Locate every Plasmodium falciparum-infected red blood cell.
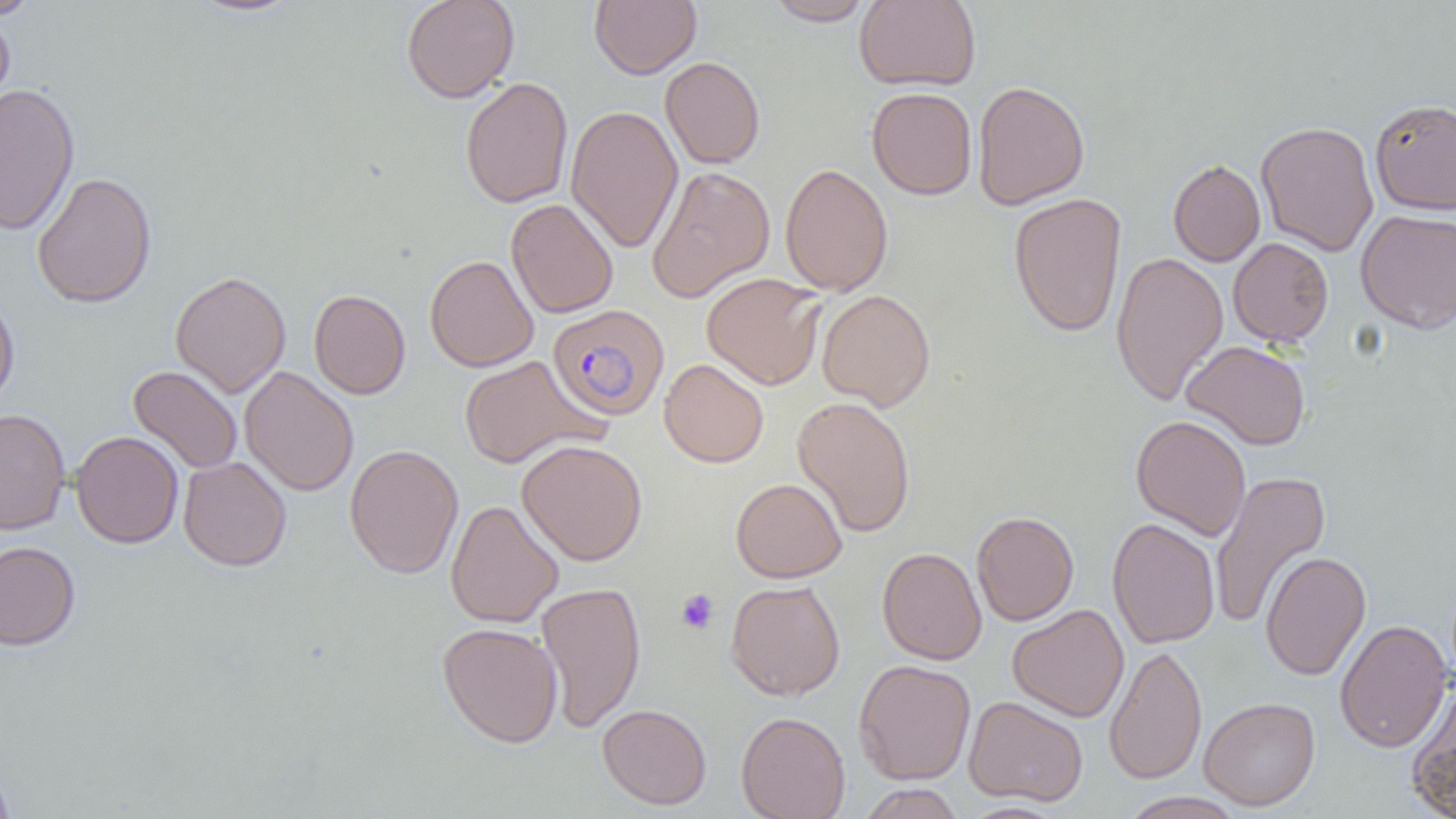

Approximate bounding boxes as [x1, y1, x2, y2] in pixels.
Plasmodium falciparum-infected red blood cells: [547, 304, 669, 422].

slide_level_diagnosis: Plasmodium falciparum
image_size: 1456×819 pixels
magnification: 1000x
uninfected_red_blood_cell_locations: 'approximate bounding boxes as [x1, y1, x2, y2] in pixels: [1, 0, 42, 20], [186, 0, 304, 17], [401, 0, 520, 103], [589, 0, 701, 79], [762, 0, 875, 26], [854, 0, 981, 91], [0, 9, 16, 114], [660, 56, 765, 169], [460, 77, 573, 209], [972, 81, 1090, 210], [0, 83, 80, 236], [866, 87, 977, 200], [1369, 99, 1456, 215], [566, 104, 683, 254], [1255, 120, 1379, 257], [1168, 159, 1265, 267], [780, 163, 893, 296], [646, 164, 775, 302], [32, 171, 157, 309], [1008, 192, 1127, 338], [506, 198, 618, 319], [1355, 209, 1456, 335], [1228, 237, 1334, 346], [1111, 251, 1228, 407], [424, 254, 539, 372], [170, 271, 291, 398], [701, 272, 826, 391], [309, 289, 411, 399], [817, 289, 936, 411], [0, 291, 20, 408], [1181, 340, 1310, 450], [459, 355, 603, 469], [658, 358, 769, 468], [127, 365, 243, 475], [239, 366, 359, 497], [791, 396, 916, 538], [0, 408, 70, 535], [1131, 415, 1251, 541], [70, 430, 183, 549], [516, 439, 648, 566], [72, 444, 291, 556], [344, 444, 464, 579], [178, 456, 292, 571], [1210, 470, 1330, 630], [731, 478, 847, 583], [445, 499, 563, 629], [971, 510, 1079, 626], [1107, 518, 1220, 649], [0, 541, 80, 651], [877, 547, 987, 665], [1260, 550, 1371, 681], [725, 579, 845, 701], [535, 581, 647, 733], [1007, 604, 1129, 722], [1334, 619, 1453, 752], [437, 622, 563, 747], [1104, 644, 1207, 785], [853, 659, 975, 785], [1405, 684, 1456, 818], [963, 695, 1088, 806], [1199, 696, 1320, 811], [597, 704, 712, 810], [736, 711, 850, 819], [0, 762, 16, 819], [856, 784, 965, 819], [1118, 791, 1247, 819], [956, 801, 1069, 819]'
platelet_locations: 'approximate bounding boxes as [x1, y1, x2, y2] in pixels: [676, 588, 719, 634]'
field_of_view: one of a larger specimen
modality: optical microscopy
preparation: thin blood smear